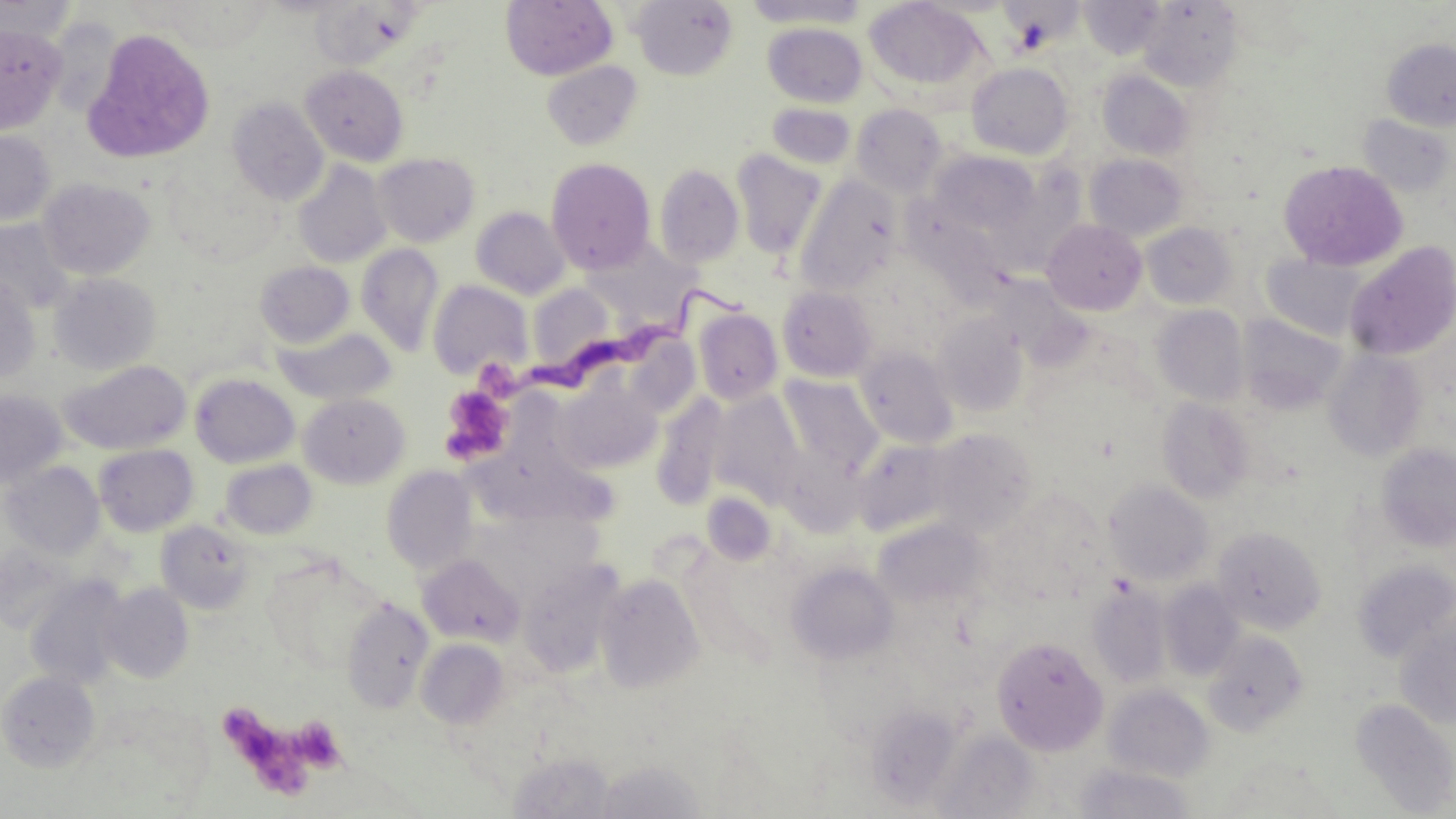
Summary:
  - Coordinate format: approximate bounding boxes as (x1,y1)-(x2,y2) corner pairs in pixels
  - Trypanosoma brucei locations: (524,285)-(751,401)
  - Platelet locations: (439,385)-(515,465), (290,717)-(347,773), (234,724)-(321,800)
  - Uninfected red blood cell locations: (501,0)-(618,80), (631,0)-(739,80), (742,0)-(869,28), (864,0)-(988,95), (1079,0)-(1166,59), (0,1)-(79,44), (308,1)-(423,71), (1137,1)-(1244,91), (45,16)-(125,119), (763,22)-(868,107), (0,23)-(67,134), (81,28)-(216,164), (1381,38)-(1456,131), (542,60)-(643,151), (965,62)-(1074,160), (300,65)-(409,166), (1097,70)-(1195,160), (227,97)-(329,205), (766,102)-(856,170), (851,103)-(948,196), (1357,114)-(1454,197), (0,129)-(56,226), (731,149)-(827,258), (931,150)-(1038,234), (373,152)-(480,247), (1085,154)-(1189,241), (546,157)-(656,274), (1277,159)-(1408,271), (293,160)-(391,268), (654,164)-(744,267), (794,176)-(901,297), (39,178)-(155,280), (471,206)-(570,300), (0,219)-(75,315), (1042,219)-(1147,315), (1141,222)-(1237,308), (1344,240)-(1456,361), (357,244)-(444,356), (1262,254)-(1368,340), (255,261)-(355,348), (48,273)-(161,375), (0,274)-(41,386), (427,279)-(533,381), (526,282)-(616,373), (777,285)-(877,382), (1152,305)-(1250,406), (693,307)-(783,405), (932,313)-(1029,417), (1238,314)-(1347,414), (274,327)-(397,406), (855,345)-(959,448), (1323,349)-(1427,462), (60,360)-(192,455), (190,373)-(300,468), (780,375)-(884,474), (557,379)-(662,473), (0,389)-(67,489), (708,391)-(806,506), (299,392)-(410,488), (651,392)-(729,510), (1156,397)-(1254,503), (929,429)-(1035,535), (852,438)-(955,537), (1375,443)-(1456,551), (93,444)-(198,537), (220,459)-(317,541), (2,461)-(104,560), (382,465)-(479,575), (1104,480)-(1214,585), (874,518)-(990,611), (155,519)-(256,615), (1212,525)-(1326,634), (0,543)-(79,635), (417,553)-(526,647), (264,557)-(379,674), (517,558)-(626,678), (788,561)-(899,665), (1353,561)-(1456,662), (594,572)-(705,694), (24,575)-(130,690), (1158,580)-(1245,681), (1086,581)-(1172,688), (98,583)-(194,683), (341,599)-(433,713), (1395,620)-(1456,728), (1202,630)-(1308,735), (991,635)-(1108,755), (416,638)-(510,729), (1,670)-(100,771), (1103,684)-(1214,781), (1350,699)-(1456,815), (934,729)-(1042,817), (506,751)-(619,819), (593,757)-(709,819), (1072,762)-(1196,818)
  - Slide-level diagnosis: Trypanosoma brucei
  - Image size: 1456×819 pixels
  - Field of view: single
  - Stain: May-Grünwald-Giemsa
  - Modality: optical microscopy
  - Magnification: 1000x
  - Preparation: thin blood smear